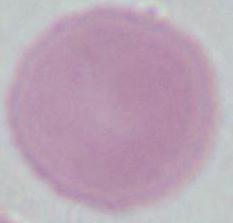

Summary:
  - Magnification: 1000x
  - Modality: photomicrograph
  - Identification: red blood cell